Classify this cell by malaria status.
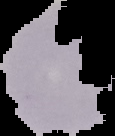
It is parasitized.

image type = segmented cell region with the area outside set to black
image size = 115×136 pixels
preparation = thin blood film